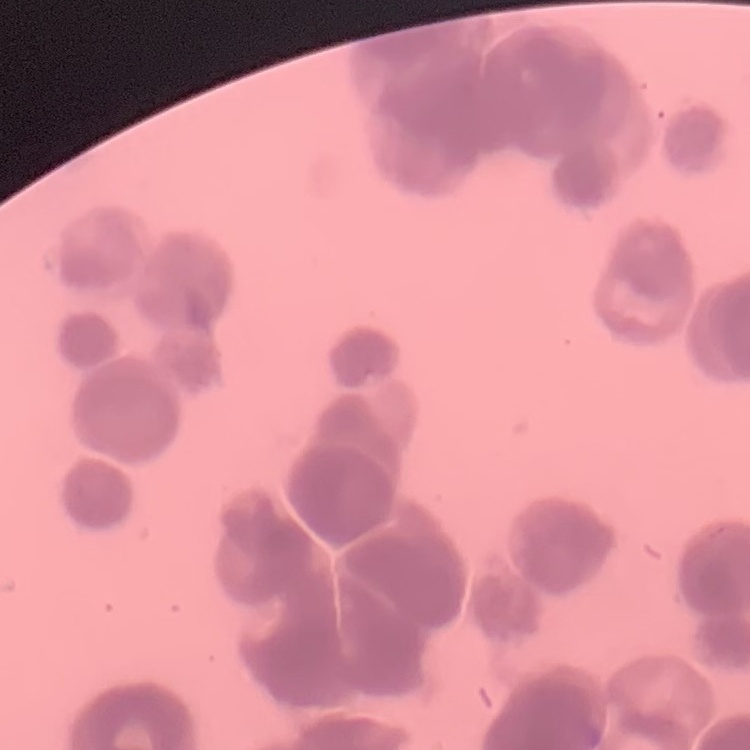
Summary:
  - Red blood cell morphology: rouleaux formation
  - Preparation: thin peripheral smear
  - Stain: Field's or Giemsa
  - Image type: square crop of a larger photomicrograph